Locate every uninfected red blood cell.
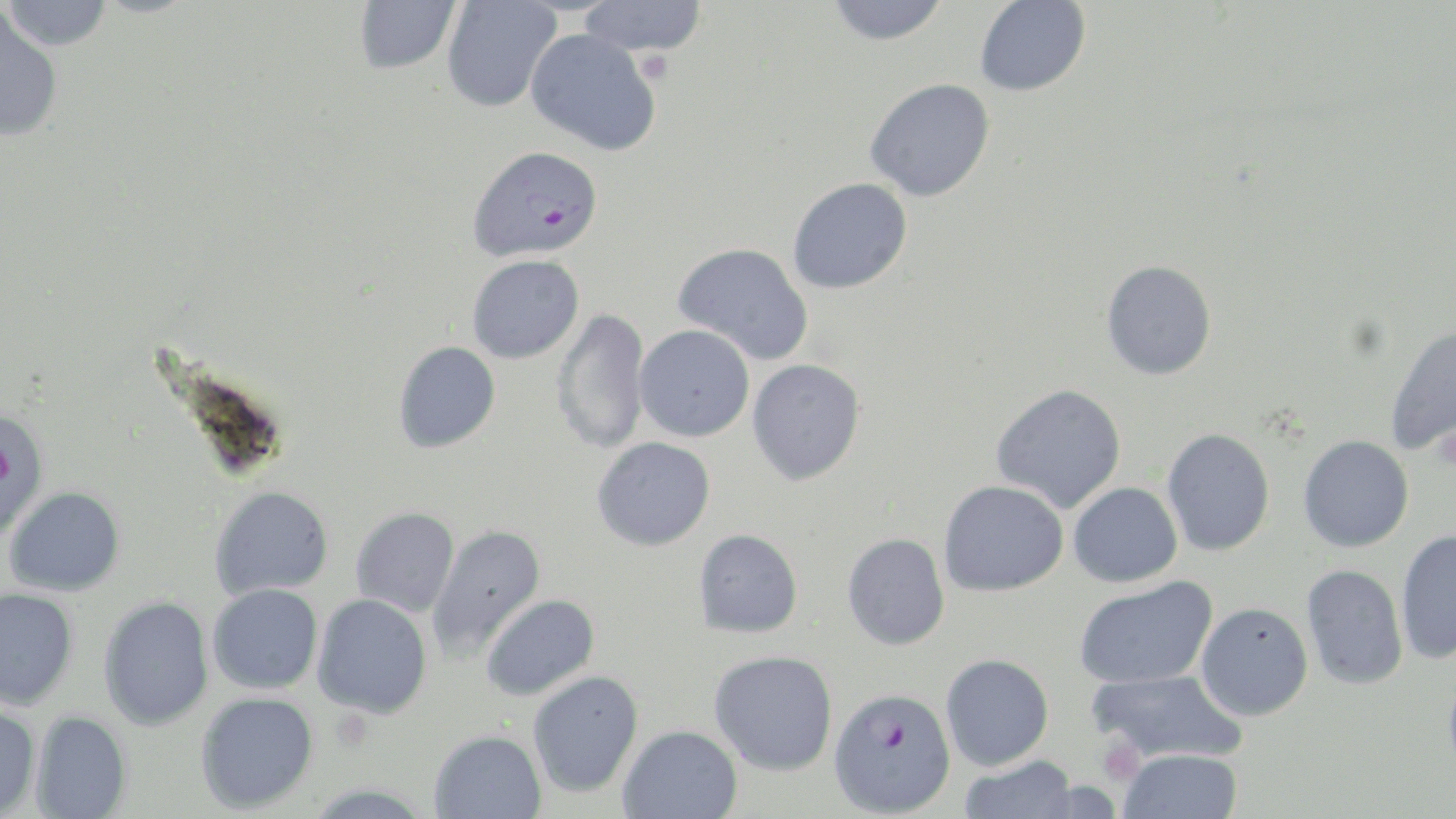

Approximate bounding boxes as (x1, y1, x2, y2) in pixels.
Uninfected red blood cells: (1, 0, 113, 51), (353, 0, 461, 75), (577, 0, 708, 57), (974, 0, 1090, 96), (441, 1, 561, 113), (825, 1, 950, 45), (0, 6, 64, 142), (525, 28, 662, 157), (864, 78, 995, 201), (787, 178, 912, 294), (672, 242, 814, 366), (467, 255, 584, 364), (1101, 260, 1217, 380), (551, 307, 651, 455), (1385, 323, 1456, 457), (634, 324, 755, 442), (393, 341, 500, 453), (747, 359, 866, 485), (990, 384, 1127, 514), (1161, 427, 1276, 557), (1297, 435, 1414, 553), (591, 437, 716, 551), (938, 480, 1069, 596), (1068, 482, 1183, 587), (4, 486, 126, 596), (209, 486, 334, 600), (350, 507, 460, 617), (427, 525, 546, 660), (693, 528, 803, 638), (1395, 530, 1456, 664), (841, 533, 950, 651), (1300, 564, 1408, 690), (1073, 576, 1217, 690), (207, 583, 324, 695), (0, 587, 79, 710), (312, 594, 432, 719), (481, 594, 599, 701), (98, 596, 214, 731), (1196, 602, 1313, 721), (709, 650, 838, 776), (940, 653, 1054, 770), (1442, 660, 1456, 788), (1087, 668, 1248, 765), (527, 670, 643, 798), (195, 690, 319, 814), (0, 703, 41, 818), (30, 710, 133, 819), (617, 724, 743, 818), (428, 729, 546, 819), (1116, 748, 1243, 818), (957, 754, 1080, 818).

slide-level diagnosis = Plasmodium falciparum
magnification = 1000x
field of view = single
preparation = thin blood smear
Plasmodium falciparum-infected red blood cell locations = approximate bounding boxes as (x1, y1, x2, y2) in pixels: (468, 145, 603, 261), (0, 406, 50, 540), (827, 686, 956, 816)
stain = May-Grünwald-Giemsa
modality = light microscopy
platelet locations = approximate bounding boxes as (x1, y1, x2, y2) in pixels: (1096, 734, 1145, 784)
image size = 1456×819 pixels